Outline each Plasmodium falciparum-infected red blood cell.
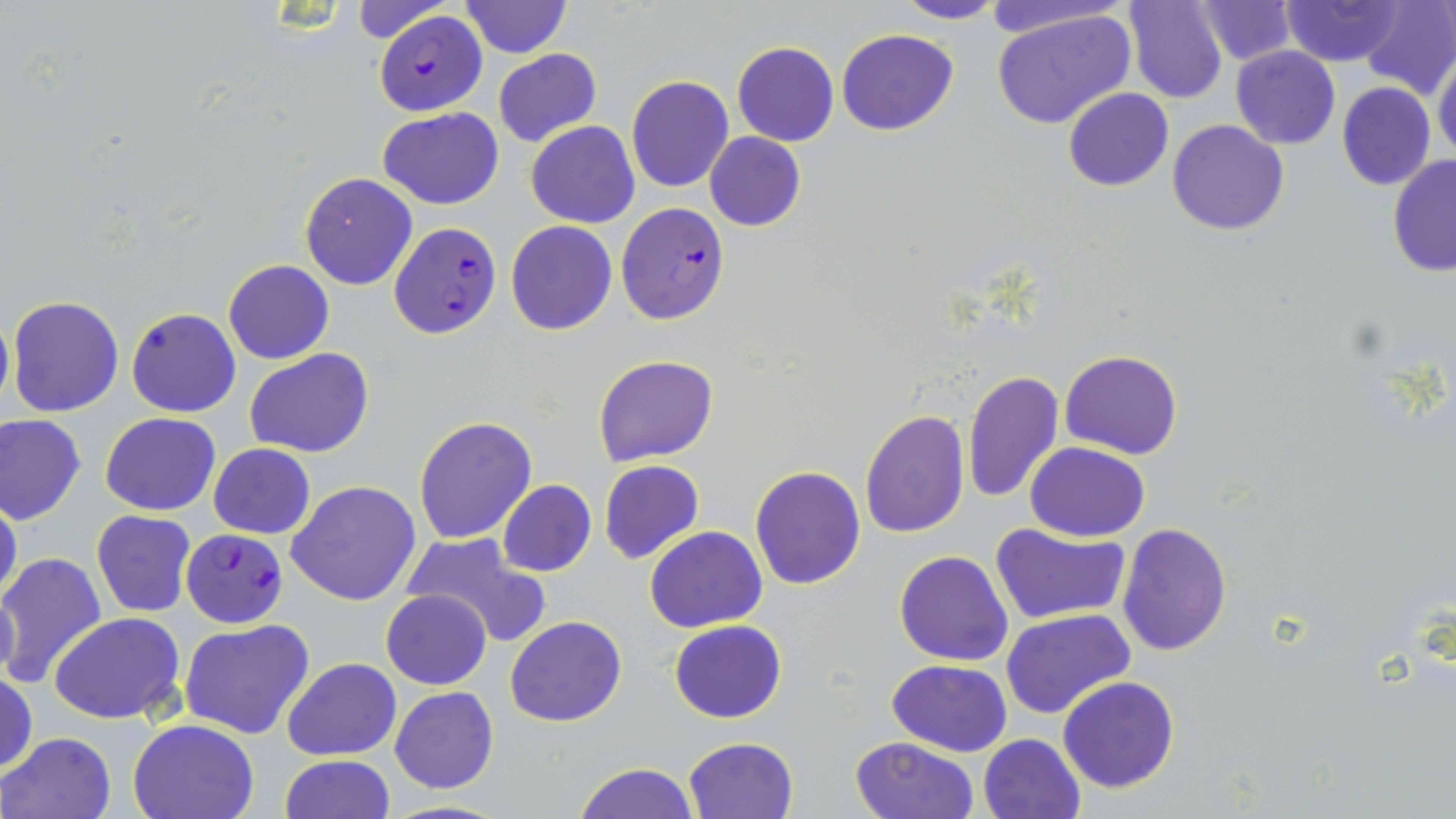
Approximate bounding boxes as (x1,y1)-(x2,y2) corner pairs in pixels.
Plasmodium falciparum-infected red blood cells: (374,11)-(487,115), (616,202)-(731,324), (387,221)-(502,339), (181,527)-(288,628).

Uninfected red blood cell locations: (348,0)-(450,42), (892,0)-(1007,25), (980,0)-(1135,40), (1125,0)-(1227,104), (1192,0)-(1296,67), (1279,0)-(1400,66), (1357,0)-(1456,99), (459,1)-(571,57), (992,8)-(1137,130), (836,28)-(959,136), (731,42)-(839,147), (1231,45)-(1340,150), (494,48)-(602,147), (1433,52)-(1456,164), (626,76)-(734,192), (1336,81)-(1436,190), (1064,88)-(1173,190), (379,106)-(504,209), (526,120)-(640,229), (1168,120)-(1290,236), (704,132)-(806,230), (1388,155)-(1456,275), (300,171)-(418,290), (505,220)-(617,336), (222,260)-(334,365), (7,295)-(124,417), (0,306)-(13,415), (127,307)-(241,417), (246,348)-(373,459), (1060,349)-(1182,459), (594,354)-(718,466), (962,369)-(1064,503), (860,408)-(969,540), (101,412)-(221,516), (1,414)-(87,525), (413,416)-(537,544), (209,442)-(315,540), (1024,442)-(1149,540), (599,460)-(703,564), (749,466)-(865,590), (288,480)-(422,604), (497,480)-(597,577), (0,493)-(23,610), (91,509)-(198,617), (989,521)-(1131,625), (1116,521)-(1232,655), (645,525)-(766,632), (404,532)-(552,647), (894,550)-(1013,665), (0,552)-(107,689), (381,590)-(492,690), (1002,608)-(1134,719), (49,612)-(186,725), (505,616)-(628,727), (180,618)-(314,739), (669,619)-(787,722), (281,657)-(400,760), (887,659)-(1013,755), (1,671)-(36,777), (1058,675)-(1180,793), (390,687)-(498,794), (128,717)-(259,819), (2,731)-(115,818), (978,733)-(1086,819), (682,736)-(798,819), (849,736)-(980,819), (279,754)-(396,818), (572,761)-(700,819), (379,799)-(514,818). Slide-level diagnosis: Plasmodium falciparum. May-Grünwald-Giemsa-stained preparation. Thin blood smear. One field of a larger specimen. Image is 1456×819 pixels. Captured at 1000x magnification. Light microscopy.